Comment on the morphology of the erythrocytes.
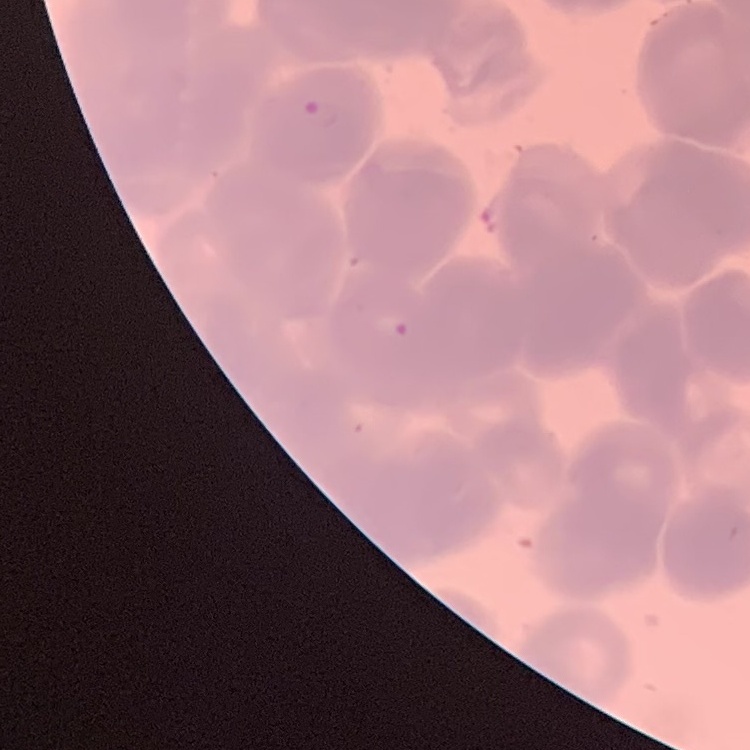

They show rouleaux formation.

One tile cut from a larger photomicrograph. Field's or Giemsa stain. Thin peripheral smear.